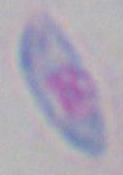

Summary:
  - Identification: Toxoplasma gondii
  - Magnification: 1000x
  - Modality: photomicrograph